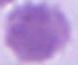
A red blood cell is shown. Photomicrograph. Captured at 1000x magnification.